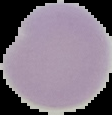
Summary:
  - Image size: 112×115 pixels
  - Result: negative for Plasmodium parasites
  - Preparation: thin blood smear
  - Image type: cell region segmented out of the field of view; surrounding area masked to black